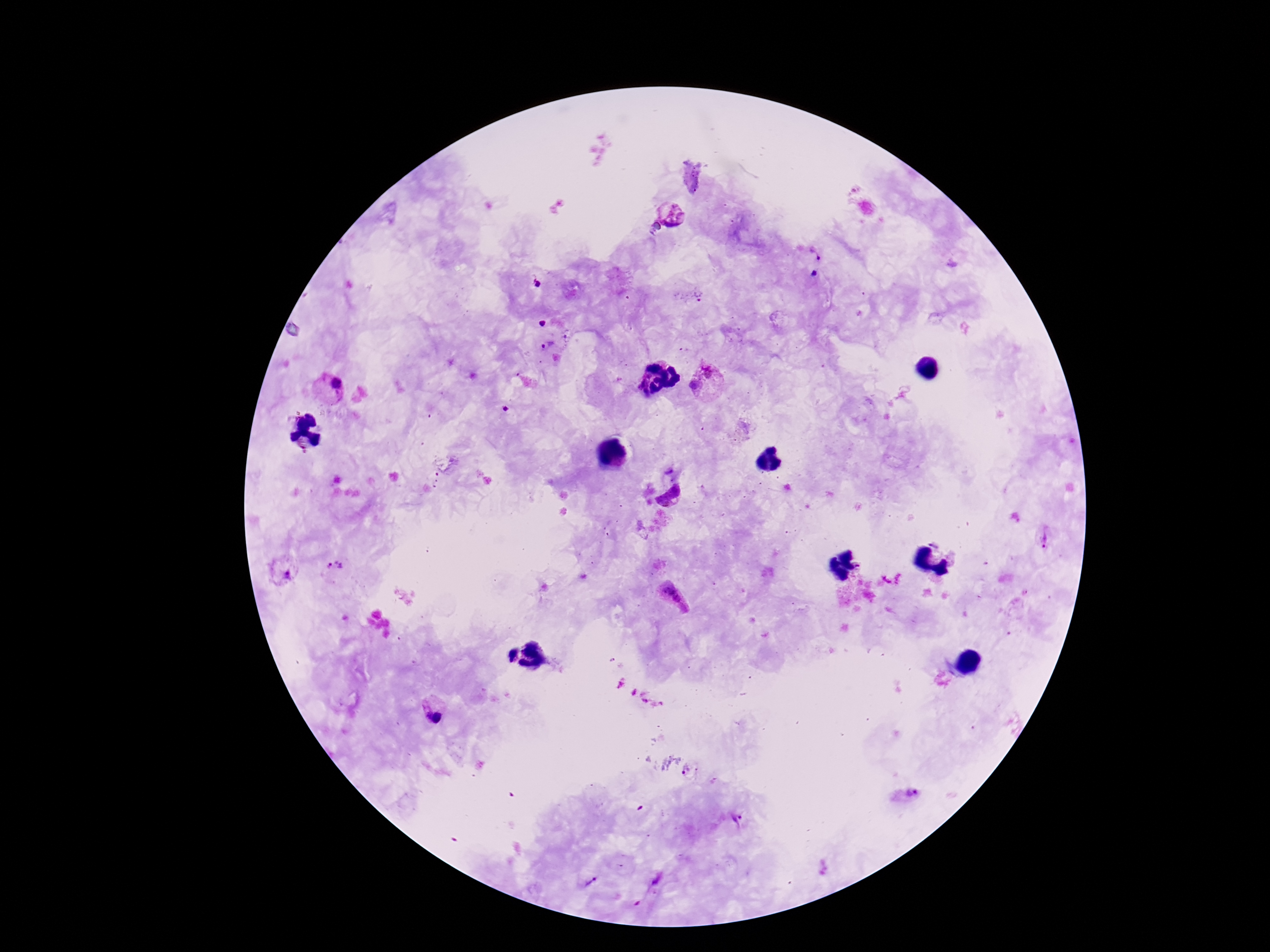

Approximate centers as (x, y) in pixels.
Summary:
  - Plasmodium parasite locations: (673, 212), (818, 257), (815, 273), (537, 285), (693, 298), (543, 323), (544, 345), (709, 369), (694, 386), (329, 388), (670, 498), (1044, 539), (935, 542), (335, 569), (284, 570), (676, 599), (434, 716), (689, 773), (908, 794), (739, 820), (657, 881), (590, 883), (637, 904)
  - Image size: 1270×952 pixels
  - Stain: Giemsa
  - Preparation: thick peripheral-blood smear
  - Capture: smartphone camera through the microscope eyepiece
  - Magnification: 100x
  - Patient malaria status: positive
  - Field of view: single